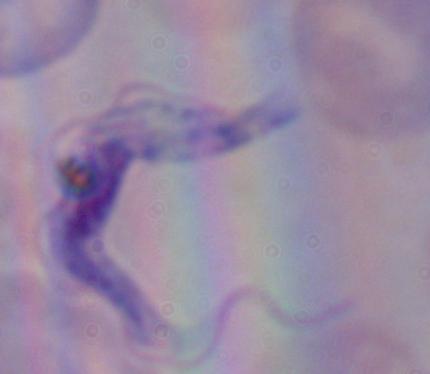
{
  "identification": "trypanosome",
  "modality": "micrograph",
  "magnification": "1000x"
}